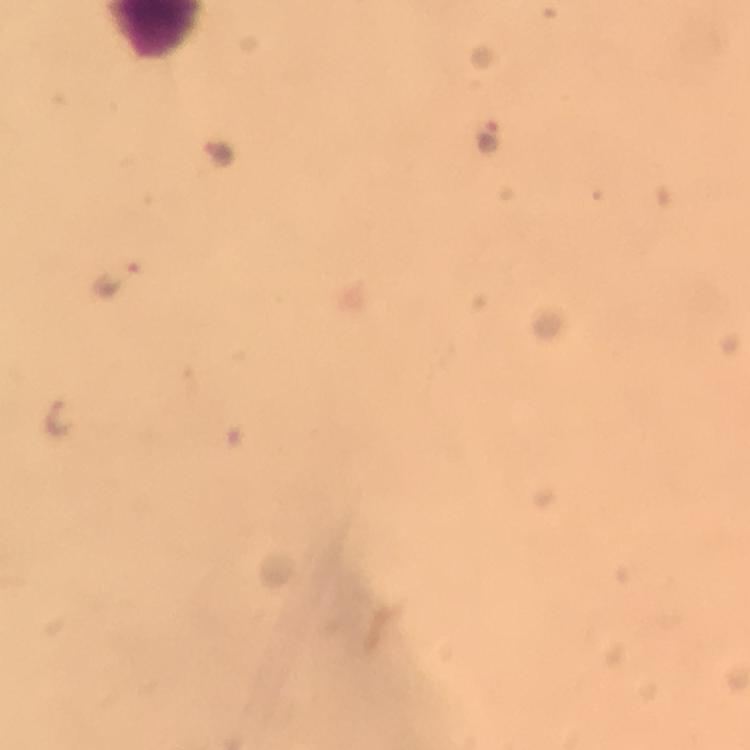 Approximate centers as {x, y} in pixels. Malaria parasite locations: {492, 138}, {216, 151}, {121, 283}, {59, 416}. Image is 750×750 pixels. From a malaria diagnostic workup. Photographed through the microscope with a smartphone camera. Thick blood film. Giemsa stain. Immersion oil was used. Cropped region of a single field of view. 100x magnification.